State which parasite is depicted.
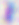
This is Toxoplasma gondii.

{
  "magnification": "400x",
  "modality": "photomicrograph"
}